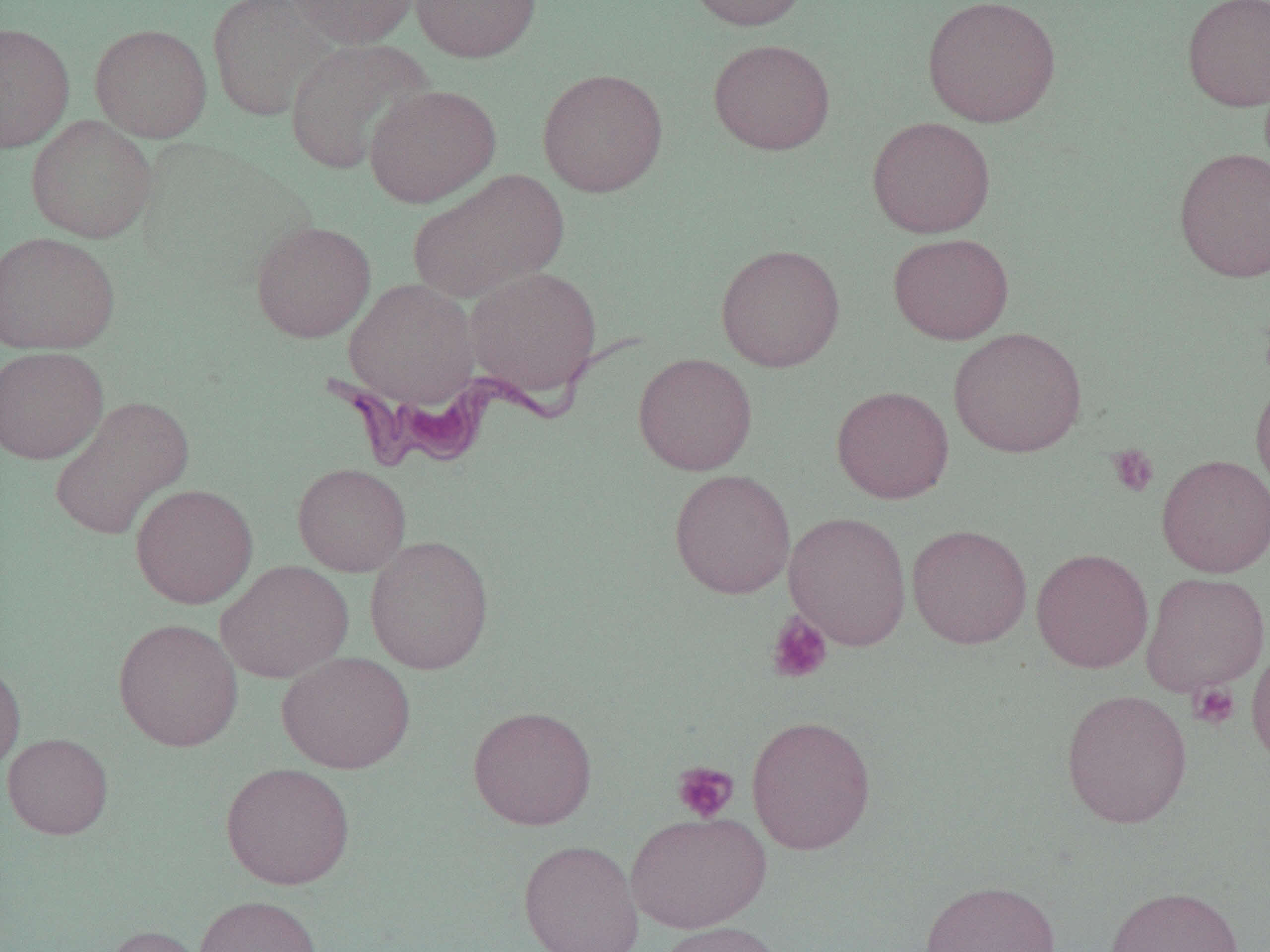
Trypanosoma brucei locations = approximate bounding boxes as [x1, y1, x2, y2] in pixels: [341, 323, 638, 473]
slide-level diagnosis = Trypanosoma brucei
preparation = thin blood film
field of view = one of a larger specimen
modality = light microscopy
uninfected red blood cell locations = approximate bounding boxes as [x1, y1, x2, y2] in pixels: [206, 0, 337, 121], [286, 0, 420, 48], [410, 0, 542, 62], [683, 0, 813, 32], [921, 0, 1061, 128], [1181, 0, 1270, 112], [0, 22, 75, 154], [90, 23, 212, 142], [284, 37, 437, 174], [708, 39, 835, 155], [537, 68, 669, 197], [364, 84, 501, 207], [26, 115, 157, 243], [867, 116, 996, 238], [1172, 146, 1270, 282], [407, 170, 568, 303], [250, 220, 376, 342], [0, 231, 120, 355], [888, 233, 1014, 344], [715, 243, 846, 372], [464, 267, 603, 398], [344, 278, 480, 408], [948, 325, 1088, 458], [0, 346, 108, 465], [632, 352, 757, 476], [1251, 374, 1270, 503], [831, 385, 954, 504], [49, 395, 195, 541], [1156, 453, 1270, 578], [292, 462, 410, 577], [669, 469, 796, 599], [130, 483, 258, 609], [783, 511, 912, 651], [907, 523, 1032, 649], [364, 535, 494, 675], [1031, 547, 1153, 673], [215, 560, 354, 683], [1140, 572, 1269, 696], [113, 617, 244, 752], [1247, 639, 1270, 768], [276, 651, 415, 774], [0, 659, 26, 774], [1060, 688, 1193, 828], [467, 705, 597, 830], [746, 714, 877, 855], [2, 733, 114, 839], [220, 762, 355, 890], [625, 811, 770, 933], [518, 839, 644, 952], [920, 880, 1061, 952], [1103, 885, 1244, 952], [194, 894, 323, 952], [656, 920, 791, 952], [101, 923, 209, 952]
image size = 1270×952 pixels
magnification = 1000x
platelet locations = approximate bounding boxes as [x1, y1, x2, y2] in pixels: [1107, 444, 1160, 497], [766, 612, 833, 685], [1188, 681, 1240, 729], [672, 761, 739, 823]